Classify this cell by malaria status.
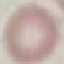

Uninfected.

{
  "preparation": "thin smear",
  "image_type": "automatically extracted cell patch, resized to 64 × 64 pixels",
  "stain": "Giemsa",
  "capture": "smartphone camera at the microscope eyepiece"
}